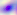
Summary:
  - Identification: Toxoplasma gondii
  - Magnification: 400x
  - Modality: photomicrograph